Classify this cell by malaria status.
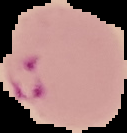
It is parasitized.

Cell region segmented out of the field of view; the surrounding area is masked to black. From a thin blood film. Image is 127×133 pixels.